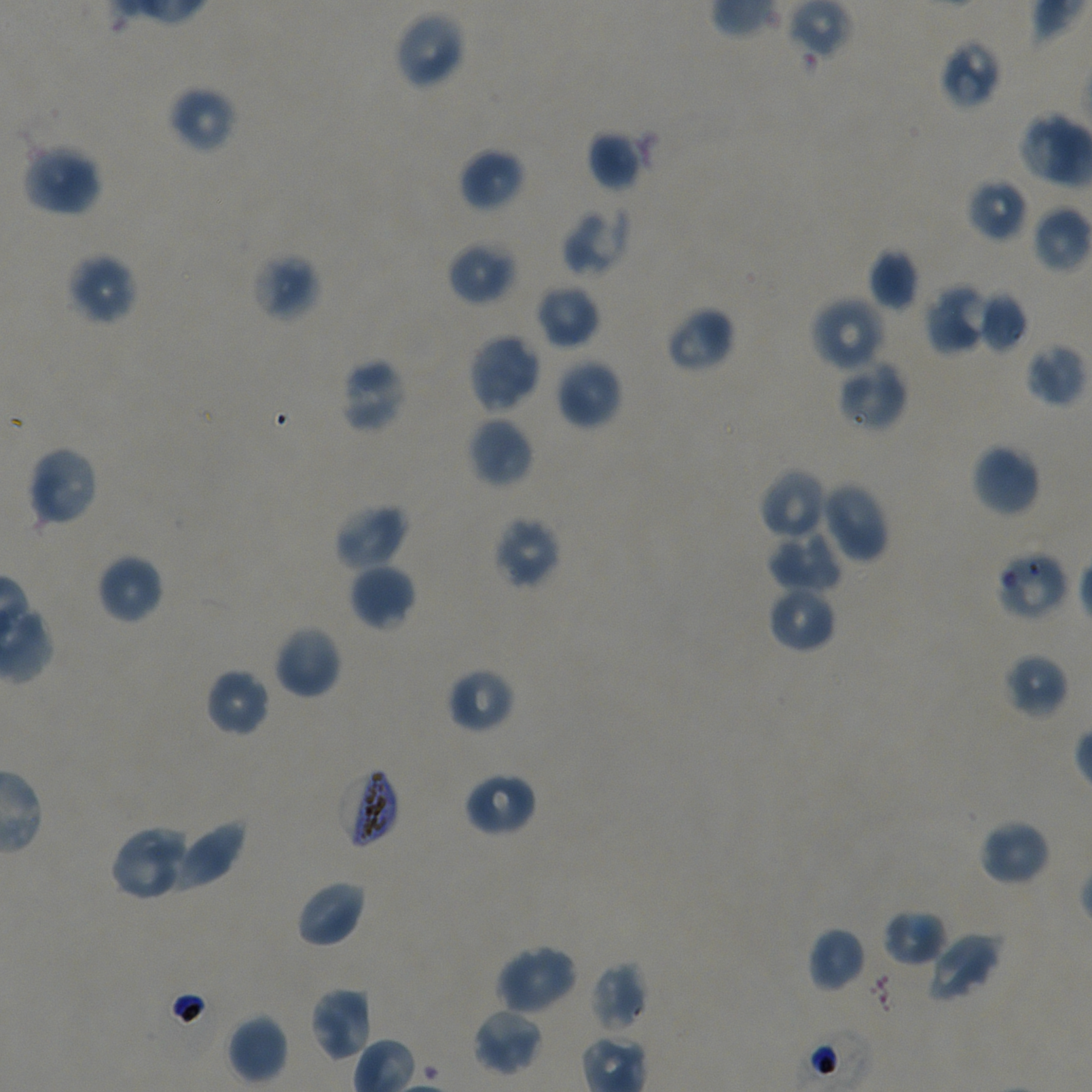

Not every red blood cell is marked.
preparation = thin blood smear
field of view = single
locations of uninfected red blood cells = approximate bounding boxes as (x1, y1, x2, y2) in pixels: (393, 10, 467, 90), (939, 37, 1003, 109), (166, 86, 237, 153), (1017, 112, 1092, 189), (587, 129, 645, 192), (22, 143, 103, 217), (458, 147, 525, 212), (967, 178, 1029, 242), (561, 206, 630, 277), (1032, 206, 1092, 274), (446, 241, 517, 306), (868, 249, 920, 310), (252, 251, 321, 323), (66, 252, 138, 327), (925, 282, 990, 355), (535, 284, 600, 348), (977, 291, 1029, 352), (810, 296, 888, 373), (666, 306, 735, 373), (467, 332, 541, 415), (1025, 343, 1088, 408), (339, 357, 407, 433), (555, 358, 623, 430), (837, 359, 908, 433), (467, 416, 534, 488), (970, 442, 1042, 517), (25, 445, 100, 528), (758, 467, 828, 541), (819, 481, 890, 564), (333, 502, 409, 571), (491, 515, 562, 590), (767, 530, 843, 594), (96, 553, 164, 624), (348, 563, 416, 631), (767, 585, 837, 653), (273, 623, 342, 699), (1002, 653, 1069, 720), (447, 667, 515, 733), (204, 668, 270, 738), (463, 771, 536, 837), (170, 818, 247, 890), (978, 818, 1051, 886), (109, 824, 195, 901), (295, 879, 367, 949), (882, 909, 947, 966), (807, 927, 866, 992), (925, 932, 1002, 1004), (494, 944, 578, 1017), (590, 962, 649, 1033), (309, 985, 374, 1062), (471, 1006, 543, 1076), (226, 1014, 288, 1085)
objective = 100x, oil immersion, numerical aperture 1.45
donor blood group = A+/O+
culture = in-vitro Plasmodium falciparum strain NF54, static
locations of red blood cells of indeterminate infection status = approximate bounding boxes as (x1, y1, x2, y2) in pixels: (996, 548, 1070, 622)
locations of infected red blood cells = approximate bounding boxes as (x1, y1, x2, y2) in pixels: (337, 764, 400, 849)
image size = 1092×1092 pixels
stain = Giemsa